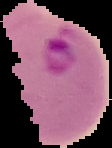

Summary:
  - Malaria status: parasitized
  - Image type: segmented cell region on a black background
  - Image size: 112×148 pixels
  - Preparation: thin blood film